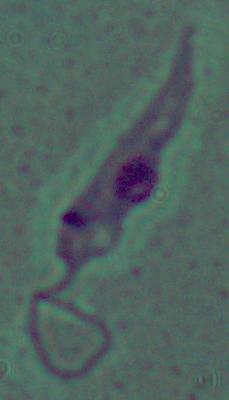

Summary:
  - Magnification: 1000x
  - Identification: Leishmania
  - Modality: micrograph